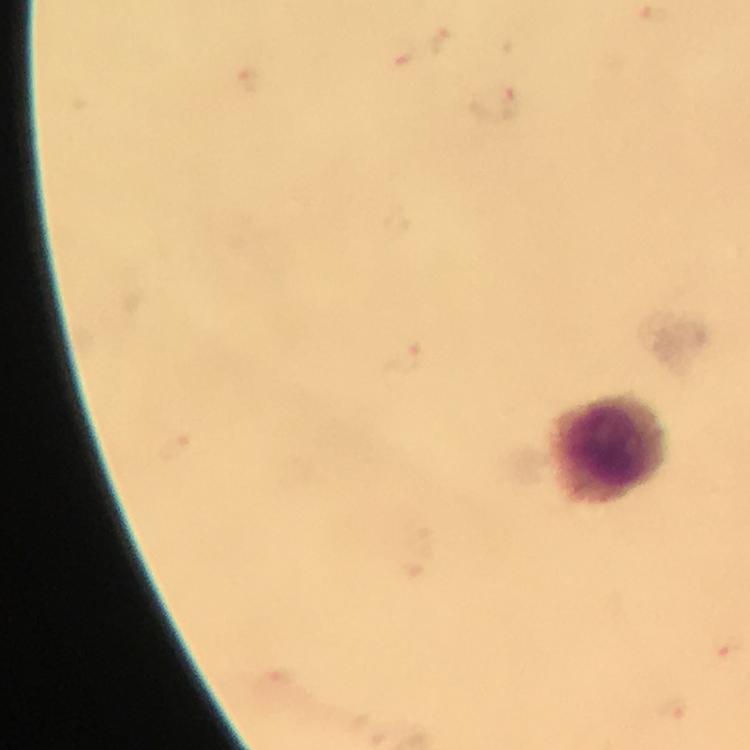 Approximate centers as {x, y} in pixels. Leukocyte locations: {607, 448}. Thick blood film. Image is 750×750 pixels. From a diagnostic examination for malaria. At 100x magnification. Malaria parasites: none detected. Photographed through the microscope with a smartphone camera. Immersion oil applied. Giemsa stain. Cropped region of a single field of view.